Identify the cell.
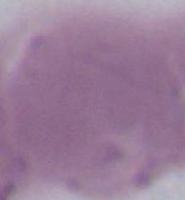
An erythrocyte.

Micrograph. Captured at 1000x magnification.